Report the malaria status of this cell.
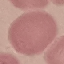
Uninfected.

Acquired by smartphone through the microscope eyepiece. Automatically extracted cell patch, resized to 64 × 64 pixels. Thin blood smear. Giemsa stain.